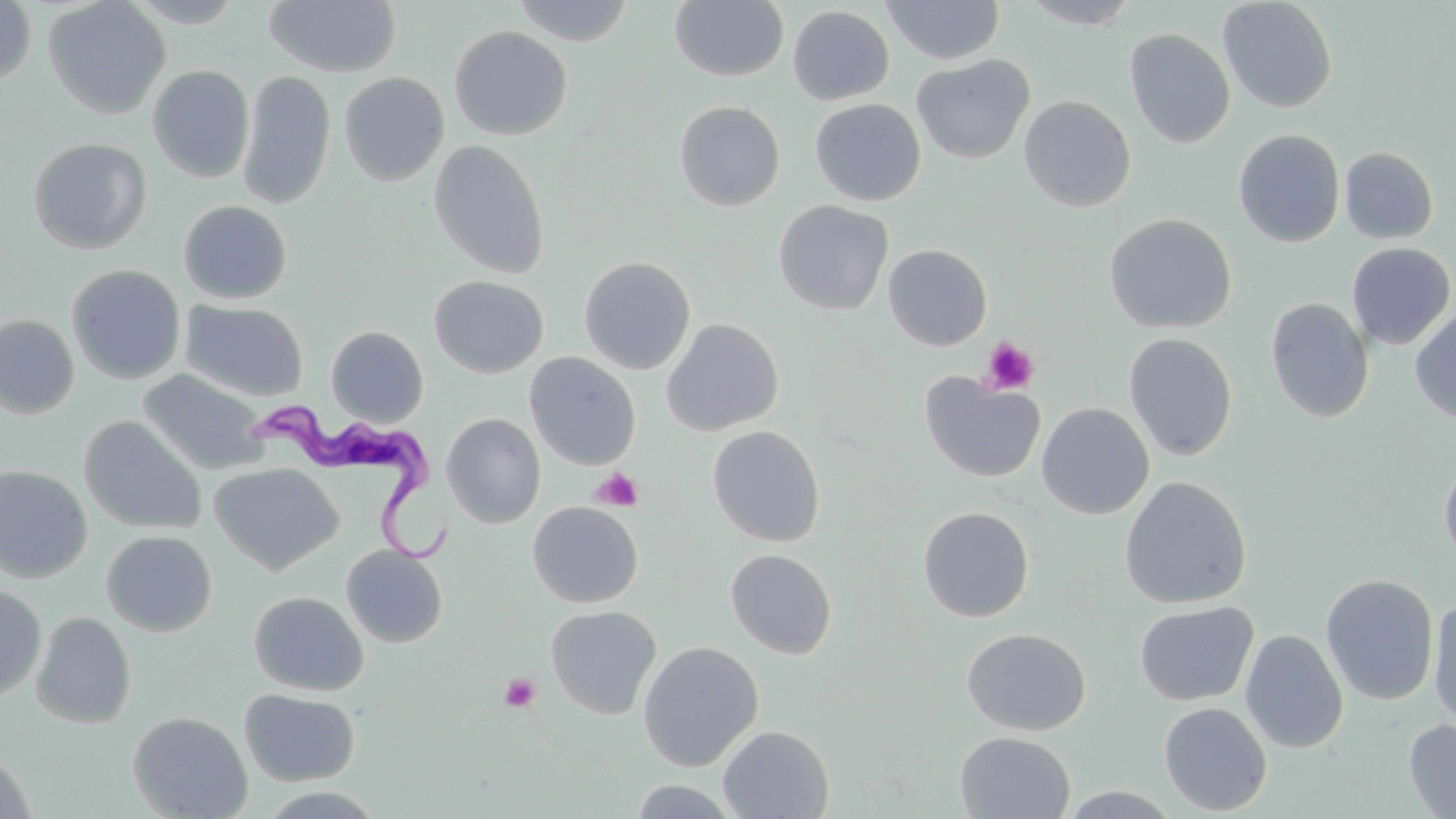

Approximate bounding boxes as [x1, y1, x2, y2] in pixels. Platelet locations: [981, 338, 1039, 395], [590, 468, 644, 512], [499, 672, 541, 714]. Trypanosoma brucei locations: [244, 400, 457, 565]. Uninfected red blood cell locations: [43, 0, 172, 119], [124, 0, 248, 27], [263, 0, 402, 77], [511, 0, 636, 46], [670, 0, 789, 82], [882, 0, 1005, 64], [1017, 0, 1143, 29], [1218, 0, 1338, 113], [0, 1, 36, 89], [787, 5, 895, 106], [449, 25, 573, 141], [1124, 28, 1235, 148], [911, 54, 1035, 165], [148, 65, 255, 183], [237, 70, 335, 210], [338, 72, 450, 187], [1019, 95, 1136, 212], [810, 98, 926, 205], [674, 100, 786, 212], [1233, 129, 1346, 248], [27, 137, 152, 254], [427, 139, 551, 280], [1339, 146, 1438, 244], [773, 199, 893, 316], [178, 200, 292, 304], [1103, 213, 1237, 334], [1346, 242, 1455, 350], [883, 244, 992, 351], [578, 256, 696, 375], [65, 264, 186, 385], [428, 275, 548, 379], [1265, 298, 1374, 423], [181, 300, 309, 401], [1410, 303, 1456, 423], [0, 314, 80, 419], [662, 317, 784, 436], [325, 325, 429, 427], [1123, 332, 1238, 461], [524, 352, 641, 471], [137, 368, 269, 475], [919, 372, 1047, 484], [1036, 402, 1155, 519], [441, 412, 546, 528], [78, 415, 207, 535], [707, 425, 826, 547], [1439, 453, 1456, 566], [209, 462, 344, 575], [0, 465, 93, 582], [1119, 476, 1252, 609], [527, 501, 643, 608], [917, 506, 1034, 622], [100, 530, 217, 637], [341, 544, 448, 648], [725, 548, 837, 660], [1320, 574, 1439, 706], [0, 586, 47, 701], [248, 591, 369, 696], [1428, 598, 1456, 731], [1134, 600, 1259, 707], [545, 604, 662, 719], [30, 611, 137, 728], [962, 627, 1091, 736], [1241, 629, 1348, 754], [637, 640, 764, 772], [239, 689, 360, 786], [1158, 701, 1273, 815], [127, 710, 253, 819], [1404, 718, 1456, 818], [718, 725, 835, 818], [954, 731, 1076, 818], [0, 750, 38, 819], [629, 779, 742, 817], [1056, 785, 1186, 817], [252, 786, 390, 818]. Slide-level diagnosis: Trypanosoma brucei. Single field of view. 1000x magnification. Light microscopy. Thin blood film. Image is 1456×819 pixels. May-Grünwald-Giemsa stain.